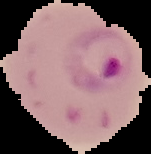 Image is 151×154 pixels. Cell region segmented out of the field of view; the surrounding area is masked to black. Malaria status: parasitized. From a thin blood smear.